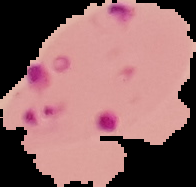

{
  "image_type": "cell region segmented out of the field of view; surrounding area masked to black",
  "preparation": "thin blood film",
  "image_size": "196×187 pixels",
  "malaria_status": "parasitized"
}